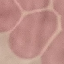
Summary:
  - Malaria status: uninfected
  - Image type: cell patch, automatically extracted from a larger field of view and resized to 64 × 64 pixels
  - Capture: smartphone through the microscope eyepiece
  - Preparation: thin blood film
  - Stain: Giemsa